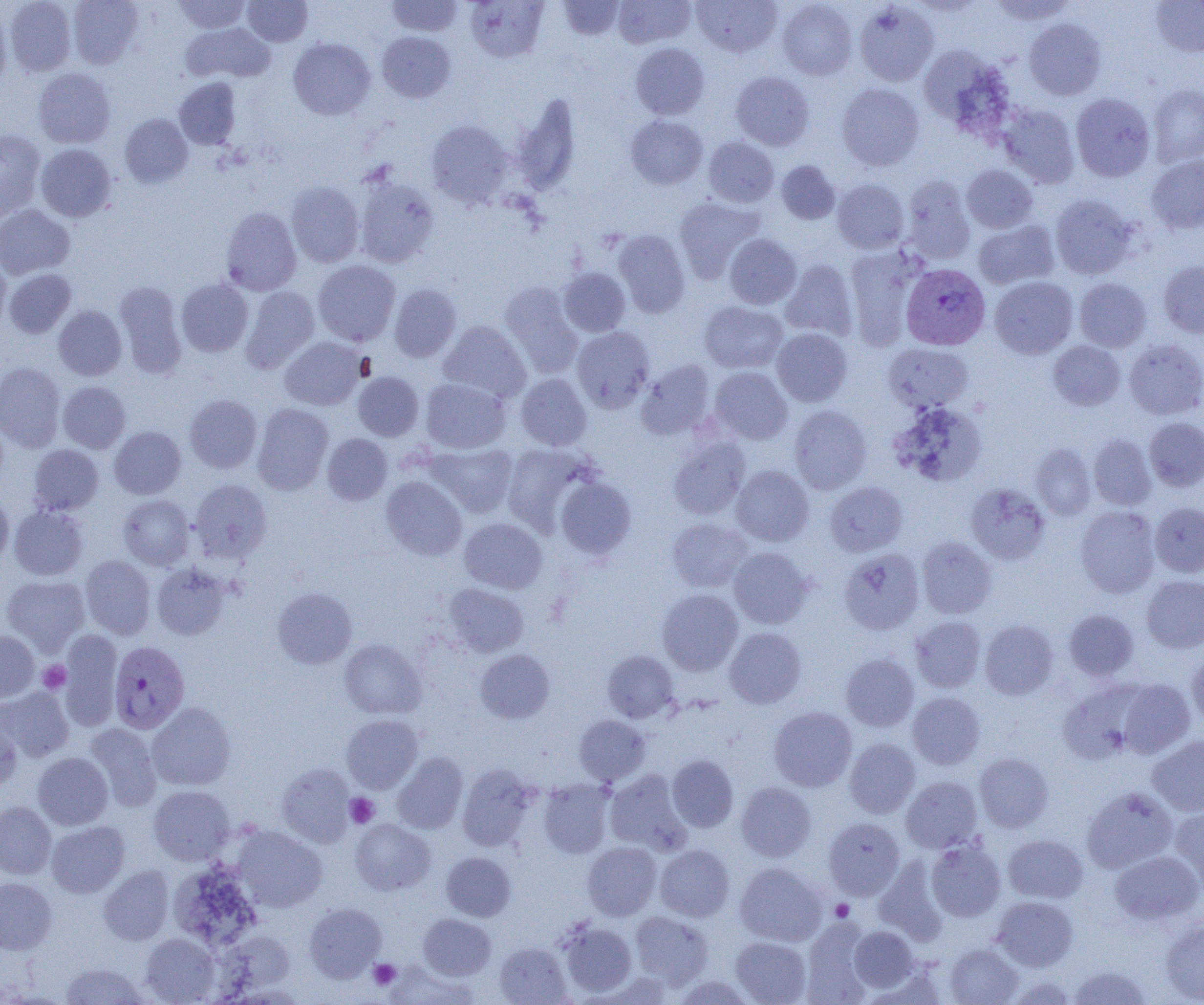
Summary:
  - Coordinate format: approximate bounding boxes as (x1,y1)-(x2,y2) corner pairs in pixels
  - Uninfected red blood cell locations: (5,0)-(76,76), (68,0)-(143,68), (172,0)-(251,33), (242,0)-(312,46), (386,0)-(464,36), (558,0)-(624,40), (613,0)-(695,48), (691,0)-(782,57), (465,1)-(549,62), (777,1)-(857,80), (988,1)-(1079,25), (1150,1)-(1204,57), (848,2)-(929,170), (854,2)-(939,86), (0,4)-(12,90), (1024,18)-(1106,100), (181,23)-(275,83), (377,32)-(455,102), (288,38)-(376,120), (630,43)-(709,120), (919,45)-(1008,130), (33,68)-(115,148), (731,71)-(814,151), (174,77)-(241,149), (837,83)-(924,170), (1148,84)-(1204,168), (1071,92)-(1155,182), (510,94)-(581,196), (997,103)-(1079,188), (120,114)-(193,188), (626,115)-(708,189), (426,120)-(513,208), (0,129)-(45,220), (703,137)-(779,207), (36,144)-(116,222), (1146,155)-(1204,234), (776,160)-(840,224), (962,165)-(1038,233), (355,176)-(439,268), (902,176)-(975,264), (832,179)-(909,254), (286,181)-(364,267), (1050,194)-(1137,279), (674,195)-(765,283), (0,204)-(74,280), (220,206)-(302,296), (973,219)-(1059,290), (613,230)-(690,317), (724,233)-(801,309), (844,247)-(922,349), (0,257)-(11,332), (780,259)-(858,340), (313,260)-(400,346), (1159,260)-(1204,338), (558,267)-(630,336), (4,269)-(76,338), (990,276)-(1078,359), (1075,278)-(1151,352), (176,279)-(253,356), (115,282)-(187,378), (500,282)-(583,378), (389,283)-(461,362), (241,286)-(319,372), (700,301)-(787,373), (54,305)-(127,380), (438,321)-(531,403), (572,326)-(655,413), (772,327)-(852,407), (280,337)-(365,410), (1124,339)-(1204,419), (1048,341)-(1125,410), (884,343)-(973,413), (636,360)-(715,440), (0,362)-(65,452), (710,366)-(792,444), (353,371)-(424,441), (516,374)-(592,451), (421,377)-(510,453), (58,381)-(130,453), (184,395)-(261,473), (252,403)-(333,495), (892,403)-(987,486), (789,406)-(872,494), (1144,417)-(1204,491), (109,426)-(185,499), (254,427)-(391,500), (323,433)-(392,505), (1089,434)-(1156,510), (668,436)-(750,519), (425,443)-(517,518), (1030,443)-(1095,520), (29,444)-(103,515), (502,444)-(594,536), (731,465)-(813,546), (381,476)-(467,560), (555,477)-(636,559), (189,479)-(272,563), (825,481)-(907,556), (966,484)-(1050,565), (0,492)-(13,566), (118,495)-(194,570), (1149,502)-(1204,577), (9,505)-(88,580), (1075,505)-(1160,598), (459,518)-(547,594), (666,518)-(752,592), (917,536)-(997,619), (728,547)-(813,629), (839,548)-(924,634), (80,554)-(155,640), (152,563)-(231,640), (1,575)-(90,655), (1142,576)-(1204,653), (444,583)-(529,657), (272,587)-(357,669), (657,589)-(743,675), (1064,609)-(1138,681), (911,616)-(985,692), (980,620)-(1058,699), (724,627)-(806,709), (0,630)-(39,702), (59,630)-(123,730), (339,639)-(426,720), (475,649)-(555,723), (602,650)-(679,722), (1186,650)-(1204,727), (841,653)-(919,731), (1117,678)-(1195,758), (1058,682)-(1145,765), (0,686)-(74,762), (908,692)-(985,769), (147,702)-(236,791), (769,706)-(857,792), (0,714)-(21,789), (341,714)-(422,793), (574,715)-(650,785), (85,723)-(162,811), (1147,735)-(1204,816), (845,738)-(920,818), (32,752)-(113,829), (392,752)-(468,834), (974,752)-(1054,832), (667,754)-(738,832), (276,764)-(355,846), (457,764)-(538,851), (604,770)-(691,855), (901,776)-(983,853), (538,779)-(613,858), (736,782)-(816,861), (149,786)-(234,865), (1081,786)-(1178,873), (0,801)-(56,879), (1170,805)-(1204,890), (824,817)-(905,900), (350,819)-(435,896), (46,821)-(129,897), (232,825)-(326,912), (1003,834)-(1088,903), (926,840)-(1006,921), (582,842)-(662,920), (655,845)-(734,921), (1110,850)-(1202,925), (441,852)-(515,921), (874,856)-(947,943), (735,862)-(827,946), (169,863)-(261,949), (99,865)-(173,945), (0,877)-(56,954), (992,896)-(1078,971), (304,903)-(386,982), (630,911)-(713,989), (418,914)-(495,979), (1161,916)-(1204,1003), (801,918)-(875,1004), (558,921)-(637,996), (849,926)-(919,992), (140,933)-(219,1004), (731,937)-(811,1005), (494,942)-(571,1004), (945,943)-(1022,1005), (61,963)-(149,1004), (383,963)-(479,1004), (1068,966)-(1151,1004), (588,972)-(676,1005), (673,975)-(754,1005), (1006,976)-(1077,1004)
  - Platelet locations: (38,660)-(71,693), (345,793)-(379,828), (831,899)-(854,922), (369,959)-(401,989)
  - Plasmodium vivax-infected red blood cell locations: (905,263)-(993,350), (110,641)-(190,733)
  - Slide-level diagnosis: Plasmodium vivax
  - Field of view: one of a larger specimen
  - Image size: 1204×1005 pixels
  - Magnification: 1000x
  - Preparation: thin blood smear
  - Modality: light microscopy